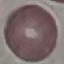
Malaria status: uninfected. Giemsa-stained preparation. Thin smear of blood. Acquired by smartphone through the microscope eyepiece. Cell patch, automatically extracted from a larger field of view and resized to 64 × 64 pixels.